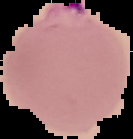
Summary:
  - Malaria status: parasitized
  - Image size: 133×139 pixels
  - Image type: cell region segmented out of the field of view; surrounding area masked to black
  - Preparation: thin blood smear